Assess the morphology of the erythrocytes.
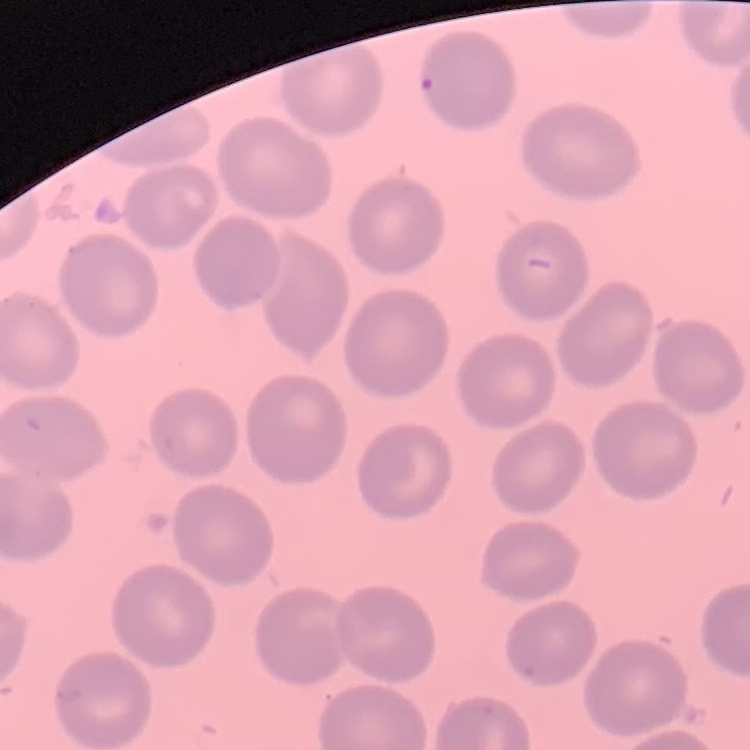

They show no rouleaux formation.

image_type: one tile cut from a larger photomicrograph
preparation: thin blood smear
stain: Field's or Giemsa